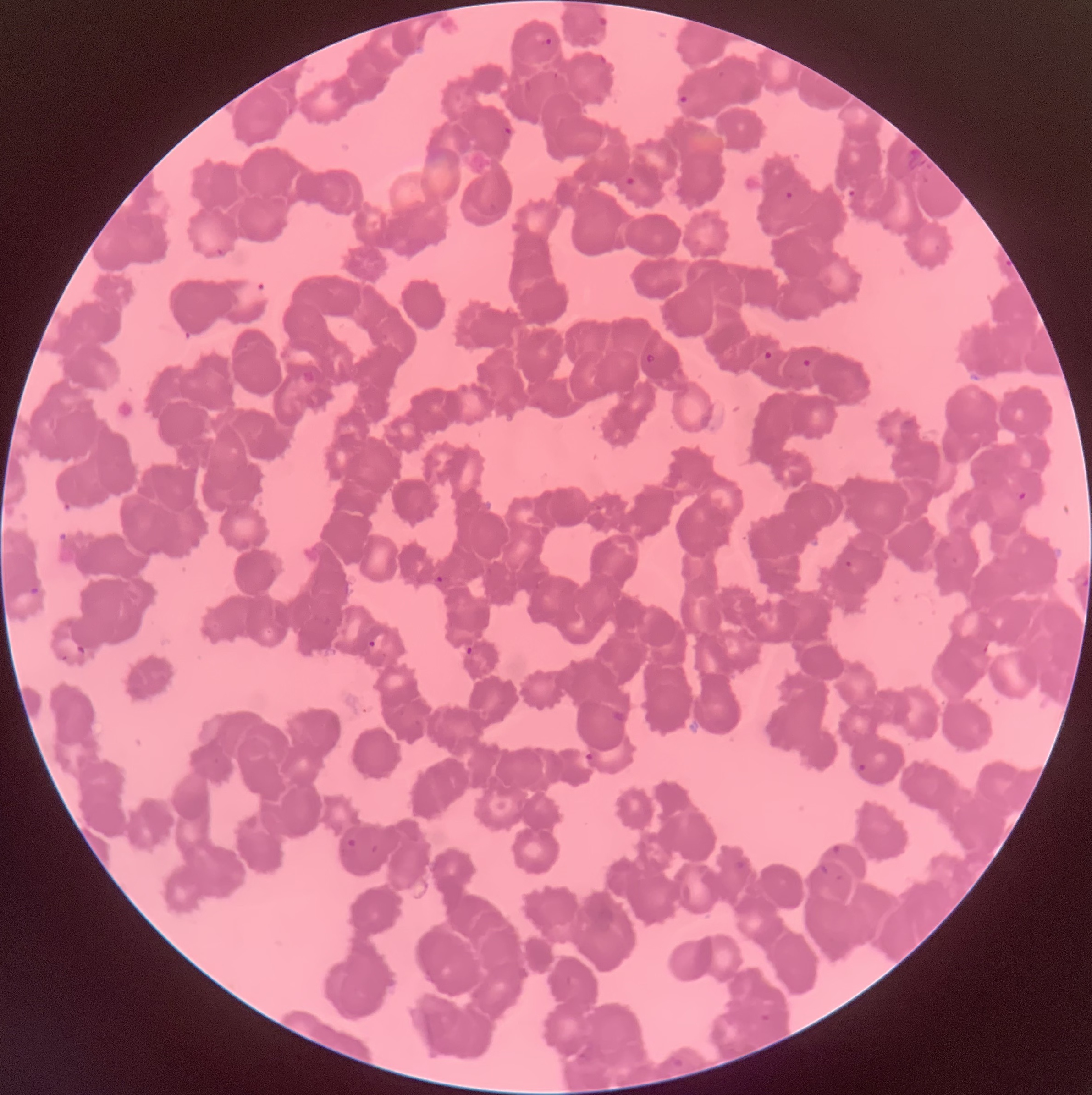

Approximate bounding boxes as [x1, y1, x2, y2] in pixels. Plasmodium parasite locations: [595, 13, 609, 29], [536, 33, 553, 47], [678, 94, 689, 106], [502, 126, 514, 138], [624, 176, 637, 188], [783, 191, 793, 201], [214, 247, 226, 257], [240, 278, 267, 304], [763, 350, 774, 361], [644, 352, 657, 365], [803, 358, 811, 368], [301, 370, 316, 385], [1016, 490, 1029, 501], [843, 559, 853, 568], [435, 575, 444, 584], [366, 640, 376, 648], [464, 646, 474, 656], [609, 708, 631, 726], [585, 750, 601, 768], [858, 762, 886, 786], [346, 838, 360, 850], [830, 843, 842, 856], [731, 859, 747, 871], [818, 863, 831, 878], [668, 1055, 685, 1069]. Optical microscopy. Thin blood smear. The red blood cells show rouleaux formation. Image is 1092×1095 pixels.